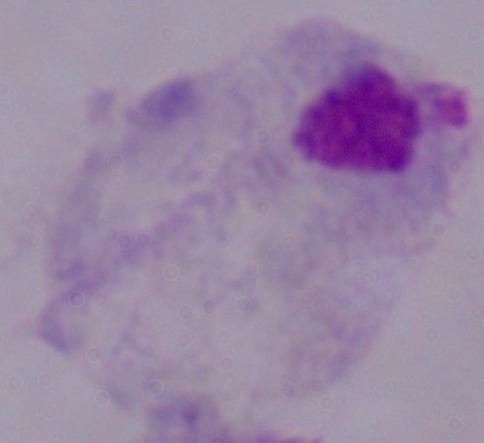
Micrograph. 1000x magnification. A trichomonad is shown.